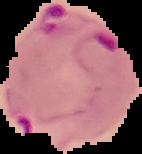
{
  "image_size": "142×154 pixels",
  "preparation": "thin blood smear",
  "image_type": "segmented cell region on a black background",
  "result": "malaria parasites identified"
}